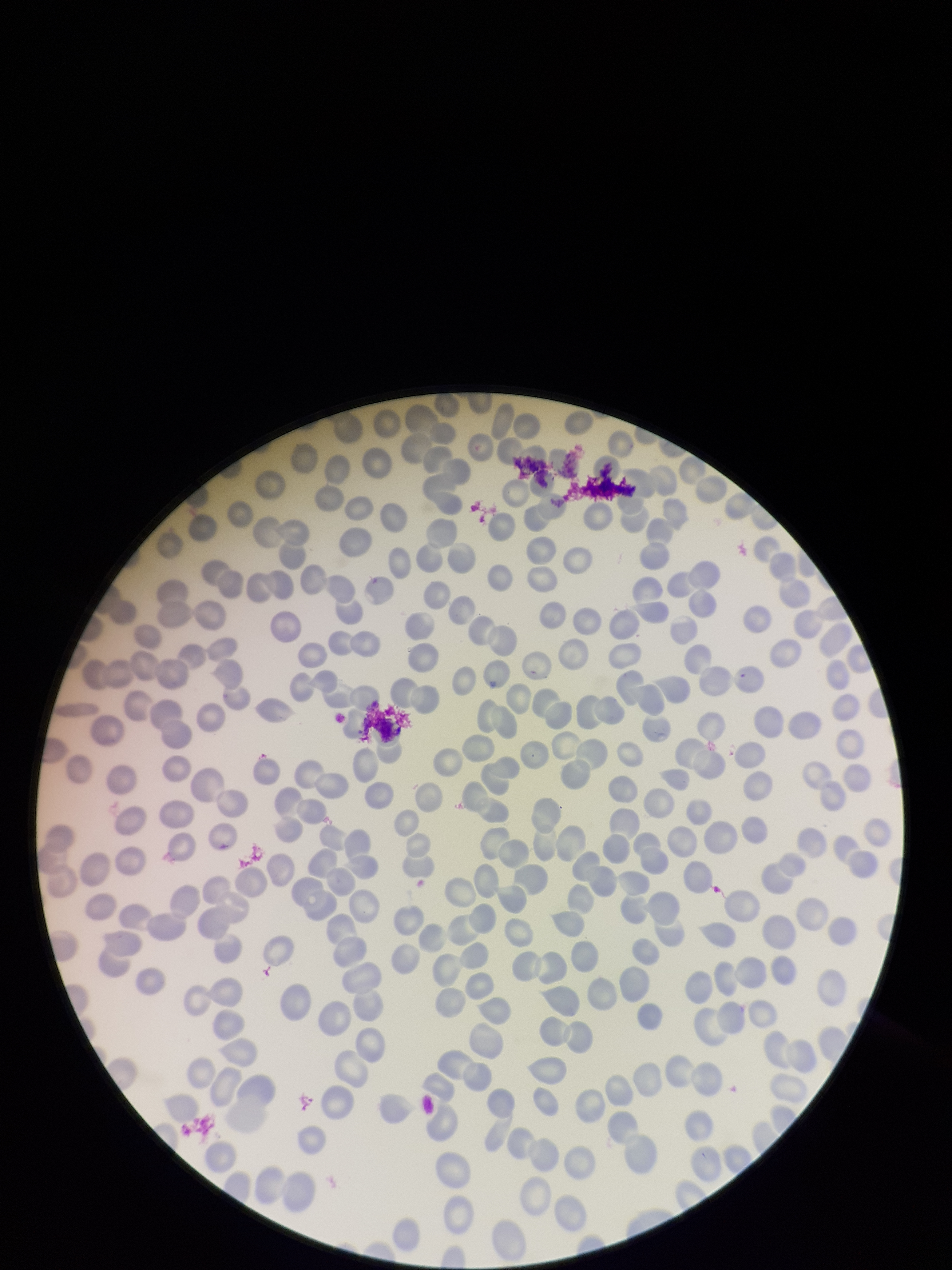
image_size: 952×1270 pixels
patient_malaria_status: negative
capture: smartphone photograph through the microscope eyepiece
parasitized_red_blood_cells: none seen
preparation: thin
stain: Giemsa
field_of_view: one from this slide
red_blood_cell_count: 247
parasitized_red_blood_cell_count: 0